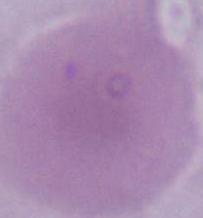
Summary:
  - Modality: photomicrograph
  - Identification: red blood cell
  - Magnification: 1000x